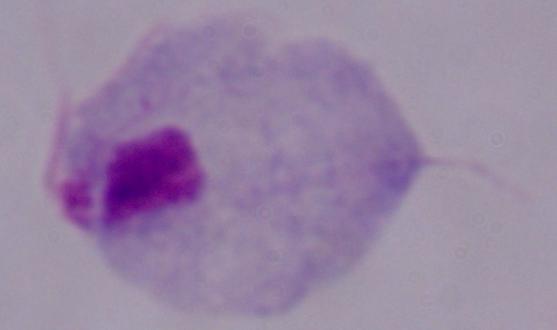

magnification: 1000x
modality: photomicrograph
identification: trichomonad